Give the extent of all uninfected red blood cells.
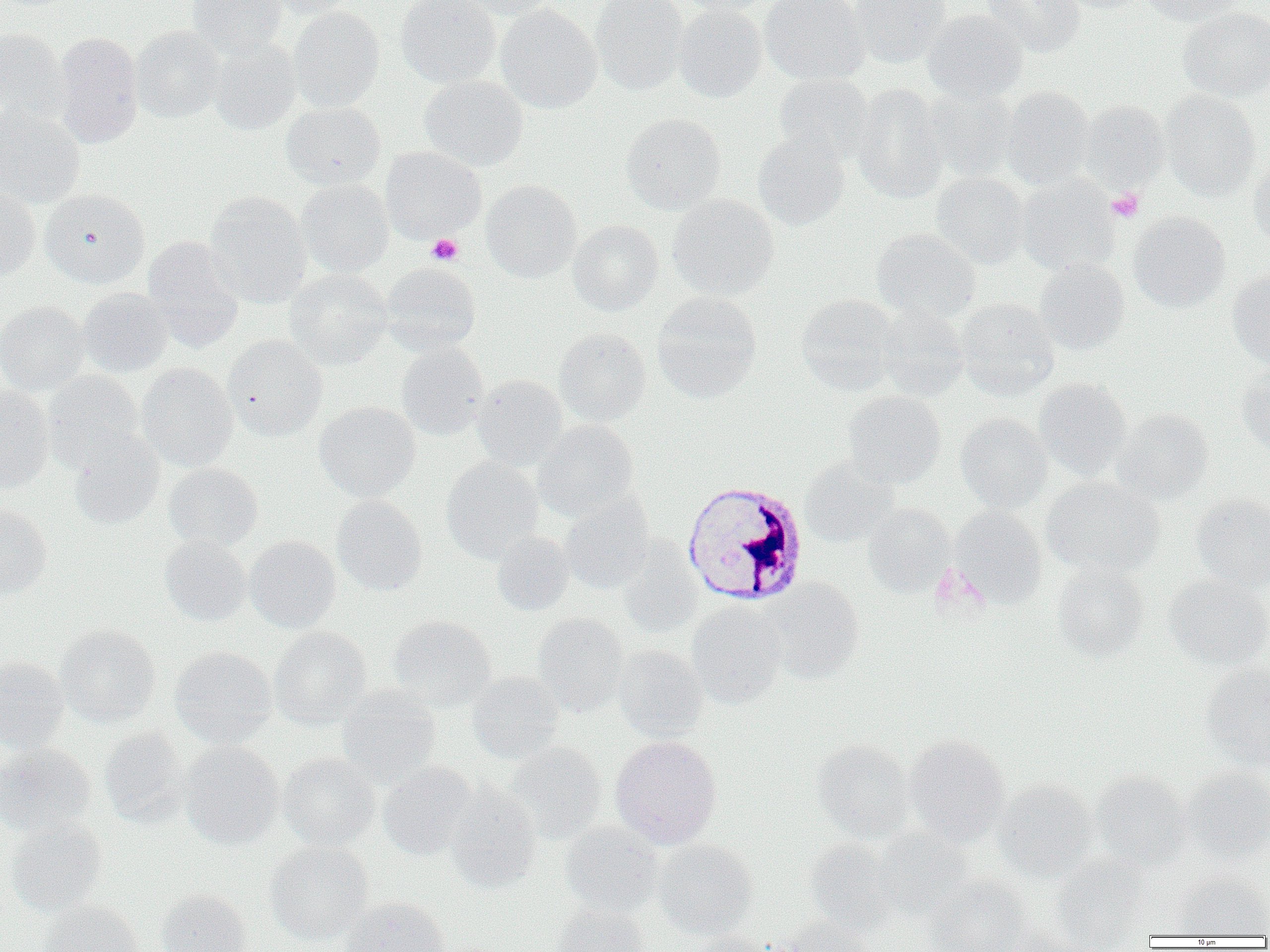
Approximate bounding boxes as [x1, y1, x2, y2] in pixels.
Uninfected red blood cells: [188, 0, 286, 57], [263, 0, 357, 18], [397, 0, 501, 88], [458, 0, 561, 19], [590, 0, 689, 95], [673, 0, 775, 16], [759, 0, 868, 85], [849, 0, 952, 68], [983, 0, 1085, 57], [1056, 0, 1148, 13], [1141, 0, 1250, 25], [673, 4, 767, 102], [496, 5, 602, 113], [288, 7, 384, 112], [1178, 7, 1270, 102], [922, 9, 1028, 103], [132, 26, 225, 122], [0, 28, 67, 126], [53, 32, 143, 148], [208, 38, 301, 135], [774, 74, 874, 164], [419, 76, 528, 171], [852, 83, 949, 202], [1001, 87, 1095, 189], [922, 88, 1018, 182], [1161, 90, 1261, 200], [1078, 100, 1168, 193], [281, 102, 385, 189], [0, 106, 85, 208], [621, 113, 726, 213], [752, 132, 849, 231], [380, 147, 486, 242], [1248, 151, 1270, 247], [931, 172, 1029, 269], [1018, 175, 1120, 276], [297, 179, 393, 277], [481, 179, 581, 282], [0, 184, 41, 279], [40, 188, 150, 288], [204, 192, 312, 309], [667, 195, 779, 300], [1128, 211, 1230, 312], [568, 220, 663, 315], [871, 229, 981, 323], [142, 237, 245, 352], [1033, 260, 1129, 354], [381, 262, 481, 354], [284, 268, 392, 369], [1227, 269, 1270, 368], [78, 288, 172, 377], [652, 292, 761, 402], [796, 294, 899, 395], [956, 298, 1060, 400], [0, 301, 90, 395], [874, 303, 968, 400], [554, 328, 651, 426], [222, 336, 328, 440], [396, 342, 489, 440], [137, 363, 238, 471], [1235, 365, 1270, 455], [42, 371, 144, 471], [472, 374, 567, 470], [1035, 379, 1132, 480], [1040, 379, 1146, 577], [0, 386, 54, 495], [842, 391, 946, 488], [315, 401, 420, 501], [1112, 408, 1213, 505], [955, 413, 1052, 513], [533, 420, 639, 520], [69, 431, 165, 530], [441, 456, 543, 563], [799, 456, 899, 547], [163, 463, 263, 551], [1042, 477, 1164, 579], [1191, 493, 1270, 591], [331, 495, 427, 596], [559, 496, 654, 593], [864, 503, 956, 596], [0, 504, 52, 602], [950, 507, 1046, 608], [492, 531, 573, 615], [160, 536, 251, 626], [245, 536, 341, 632], [618, 539, 702, 638], [1051, 563, 1149, 662], [1163, 574, 1270, 671], [1184, 574, 1270, 768], [764, 579, 865, 683], [687, 601, 786, 707], [533, 614, 629, 717], [388, 615, 496, 710], [56, 624, 160, 727], [269, 627, 372, 729], [613, 644, 708, 741], [170, 646, 276, 748], [0, 656, 69, 751], [1200, 664, 1270, 771], [467, 671, 564, 763], [337, 685, 441, 786], [99, 726, 189, 827], [904, 734, 1009, 844], [610, 735, 722, 848], [812, 740, 914, 841], [180, 742, 283, 849], [505, 742, 607, 842], [0, 743, 95, 837], [278, 752, 381, 850], [378, 760, 477, 860], [1182, 767, 1270, 864], [1091, 770, 1192, 871], [995, 779, 1098, 881], [446, 783, 542, 891], [6, 816, 107, 916], [560, 823, 664, 919], [872, 827, 974, 918], [653, 838, 757, 939], [805, 838, 897, 935], [264, 841, 373, 945], [1050, 856, 1153, 950], [1171, 873, 1269, 936], [924, 875, 1031, 952], [156, 889, 252, 952], [342, 897, 450, 952], [39, 900, 142, 952], [553, 903, 651, 952], [774, 916, 875, 952], [998, 922, 1092, 952], [686, 932, 773, 952].

Summary:
  - Platelet locations: [1107, 189, 1144, 223], [427, 234, 463, 265]
  - White blood cell locations: [681, 479, 808, 606]
  - Slide-level diagnosis: Plasmodium malariae
  - Image size: 1270×952 pixels
  - Field of view: one of a larger specimen
  - Preparation: thin blood smear
  - Magnification: 1000x
  - Modality: optical microscopy